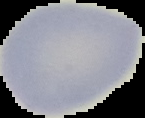

Image is 145×118 pixels. Cell region segmented out of the field of view; the surrounding area is masked to black. Result: no malaria parasites detected. From a thin blood film.